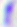
magnification: 400x
identification: Toxoplasma gondii
modality: micrograph